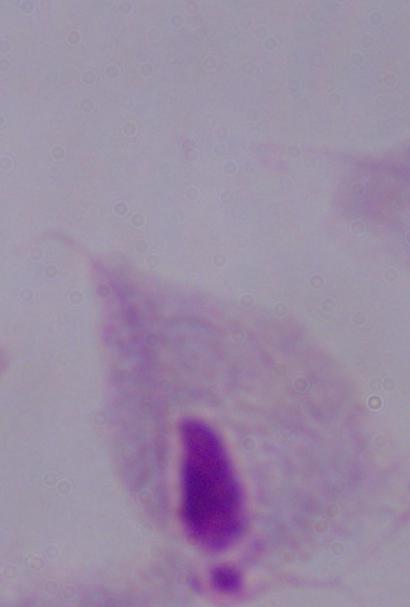 Micrograph. Captured at 1000x magnification. A trichomonad is shown.